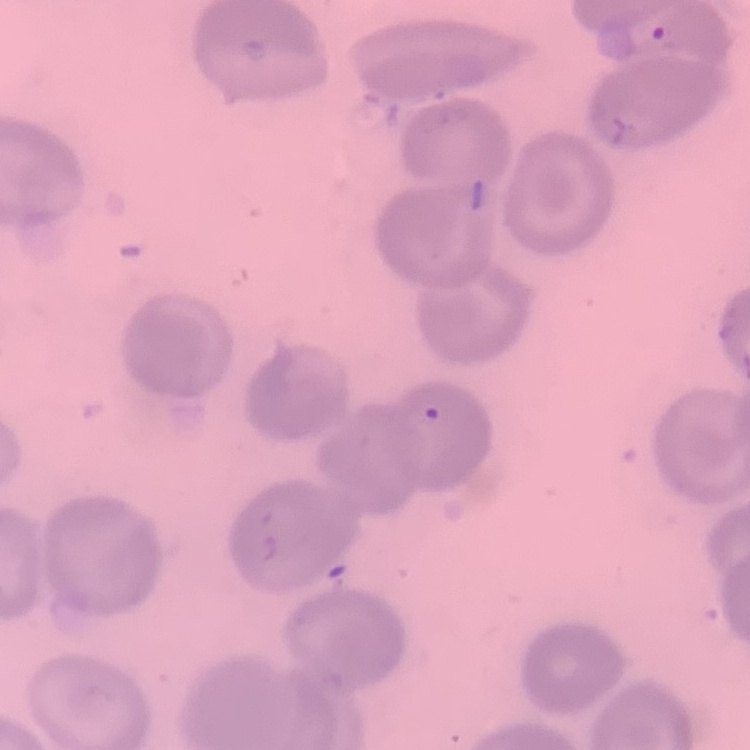

erythrocyte morphology = no rouleaux formation
stain = Field's or Giemsa
image type = one tile cut from a larger photomicrograph
preparation = thin blood smear